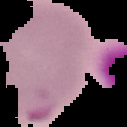
From a thin blood smear. Malaria status: parasitized. Segmented cell region on a black background. Image is 127×127 pixels.